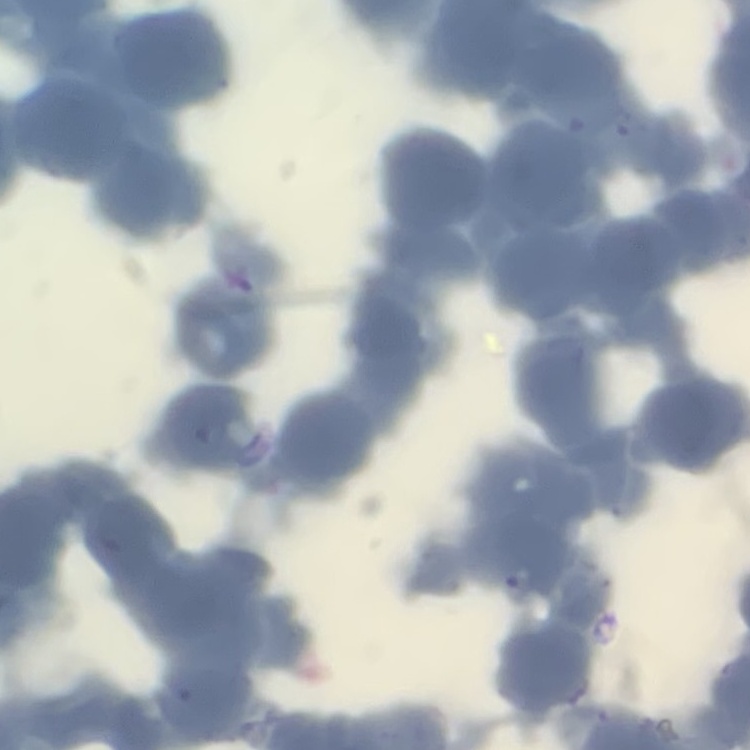
Summary:
  - Red blood cell morphology: rouleaux formation
  - Stain: Field's or Giemsa
  - Image type: one tile cut from a larger photomicrograph
  - Preparation: thin peripheral smear